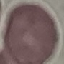

Malaria status: uninfected. Thin blood film. Giemsa stain. Acquired by smartphone through the microscope eyepiece. Automatically extracted cell patch, resized to 64 × 64 pixels.